Outline each blood parasite and name the species.
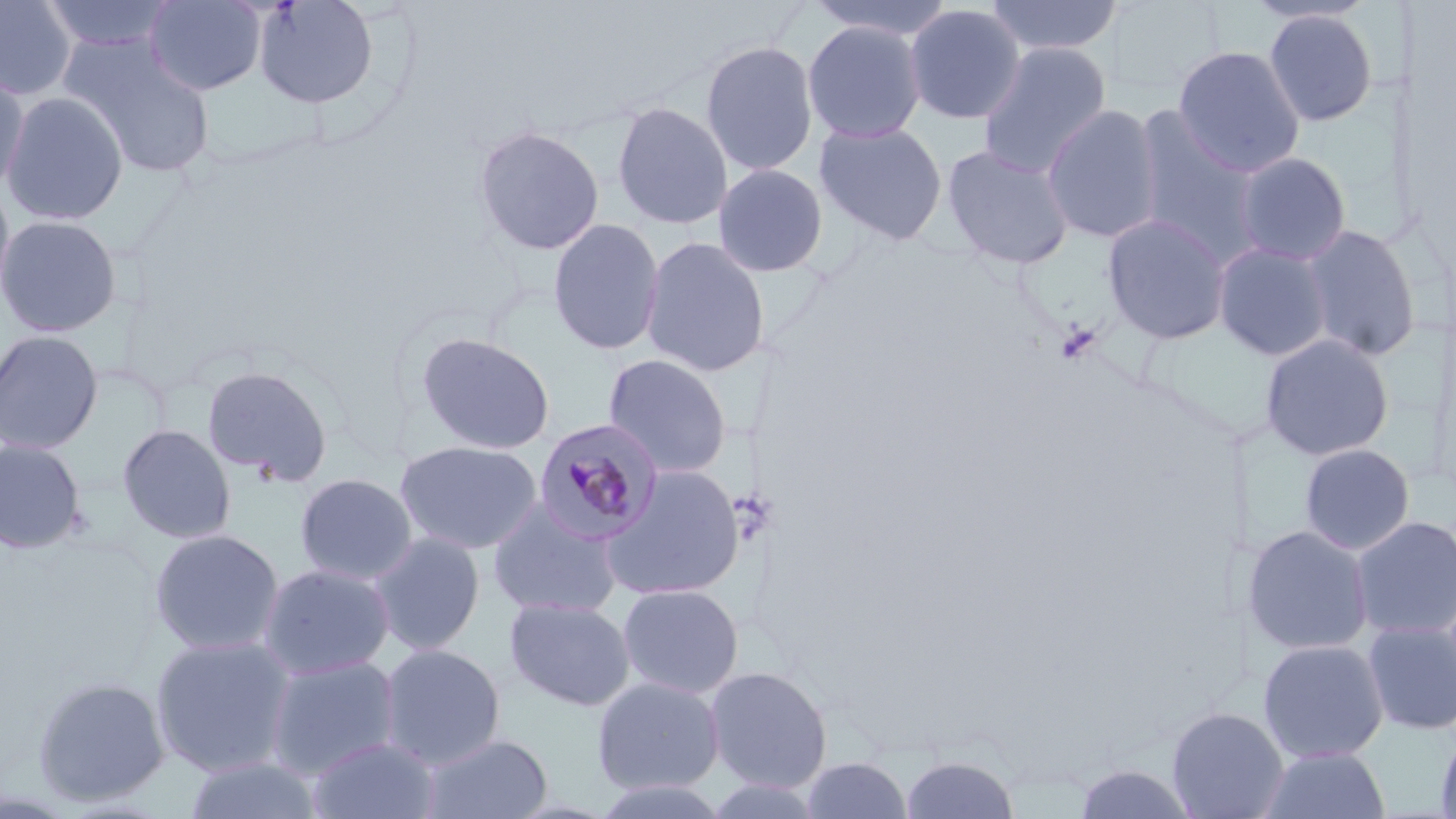

Approximate bounding boxes as named x1/y1/x2/y2 corners in pixels.
Plasmodium malariae-infected red blood cells: (x1=533, y1=418, x2=665, y2=545).
No Plasmodium falciparum, Plasmodium ovale, Plasmodium vivax, Babesia divergens, or Trypanosoma brucei observed.

Summary:
  - Platelet locations: (x1=1055, y1=321, x2=1101, y2=365)
  - Uninfected red blood cell locations: (x1=38, y1=0, x2=179, y2=55), (x1=143, y1=0, x2=267, y2=95), (x1=253, y1=0, x2=380, y2=109), (x1=807, y1=0, x2=955, y2=42), (x1=984, y1=0, x2=1125, y2=58), (x1=0, y1=1, x2=78, y2=100), (x1=903, y1=3, x2=1026, y2=125), (x1=1263, y1=8, x2=1379, y2=127), (x1=802, y1=20, x2=926, y2=143), (x1=59, y1=36, x2=215, y2=177), (x1=700, y1=39, x2=819, y2=176), (x1=977, y1=42, x2=1112, y2=180), (x1=1172, y1=44, x2=1306, y2=177), (x1=0, y1=66, x2=30, y2=197), (x1=2, y1=91, x2=129, y2=226), (x1=611, y1=101, x2=733, y2=230), (x1=1042, y1=104, x2=1163, y2=244), (x1=1129, y1=109, x2=1263, y2=262), (x1=813, y1=120, x2=949, y2=245), (x1=472, y1=124, x2=605, y2=256), (x1=942, y1=143, x2=1076, y2=270), (x1=1233, y1=151, x2=1352, y2=266), (x1=712, y1=163, x2=830, y2=278), (x1=0, y1=177, x2=17, y2=313), (x1=1102, y1=213, x2=1232, y2=344), (x1=0, y1=214, x2=123, y2=338), (x1=547, y1=218, x2=665, y2=356), (x1=1299, y1=224, x2=1422, y2=362), (x1=640, y1=236, x2=771, y2=377), (x1=1213, y1=242, x2=1332, y2=362), (x1=0, y1=330, x2=104, y2=455), (x1=416, y1=332, x2=556, y2=455), (x1=1259, y1=333, x2=1395, y2=462), (x1=602, y1=353, x2=733, y2=478), (x1=201, y1=365, x2=332, y2=485), (x1=117, y1=423, x2=236, y2=544), (x1=0, y1=438, x2=87, y2=554), (x1=394, y1=439, x2=544, y2=555), (x1=1299, y1=443, x2=1415, y2=555), (x1=600, y1=464, x2=746, y2=601), (x1=294, y1=472, x2=419, y2=585), (x1=487, y1=499, x2=625, y2=619), (x1=1350, y1=515, x2=1456, y2=641), (x1=1242, y1=524, x2=1374, y2=656), (x1=149, y1=528, x2=285, y2=656), (x1=368, y1=532, x2=486, y2=656), (x1=258, y1=563, x2=395, y2=680), (x1=617, y1=583, x2=745, y2=699), (x1=504, y1=597, x2=636, y2=711), (x1=1362, y1=620, x2=1456, y2=735), (x1=149, y1=634, x2=298, y2=777), (x1=1257, y1=639, x2=1389, y2=764), (x1=377, y1=643, x2=506, y2=769), (x1=264, y1=656, x2=401, y2=780), (x1=704, y1=665, x2=833, y2=794), (x1=32, y1=675, x2=170, y2=806), (x1=591, y1=676, x2=725, y2=795), (x1=1166, y1=706, x2=1289, y2=819), (x1=1434, y1=728, x2=1456, y2=819), (x1=419, y1=733, x2=553, y2=819), (x1=307, y1=736, x2=441, y2=819), (x1=1259, y1=746, x2=1391, y2=818), (x1=899, y1=753, x2=1020, y2=818), (x1=182, y1=756, x2=322, y2=819), (x1=798, y1=756, x2=914, y2=819), (x1=1073, y1=763, x2=1202, y2=819), (x1=588, y1=778, x2=735, y2=818)
  - Slide-level diagnosis: Plasmodium malariae
  - Magnification: 1000x
  - Stain: May-Grünwald-Giemsa
  - Preparation: thin blood film
  - Field of view: one of a larger specimen
  - Image size: 1456×819 pixels
  - Modality: light microscopy